State which parasite is depicted.
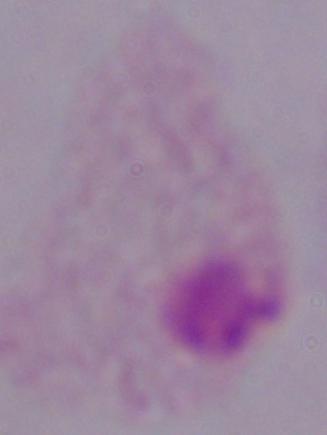

A trichomonad.

1000x magnification. Micrograph.